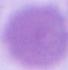

1000x magnification. An erythrocyte is shown. Micrograph.